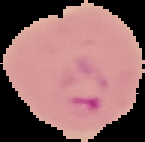
Summary:
  - Image size: 145×142 pixels
  - Result: malaria parasites identified
  - Image type: segmented cell region on a black background
  - Preparation: thin blood film